Report the malaria status of this cell.
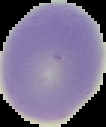
It is uninfected.

Summary:
  - Preparation: thin blood smear
  - Image type: segmented cell region with the area outside set to black
  - Image size: 106×127 pixels